Evaluate for Plasmodium parasites.
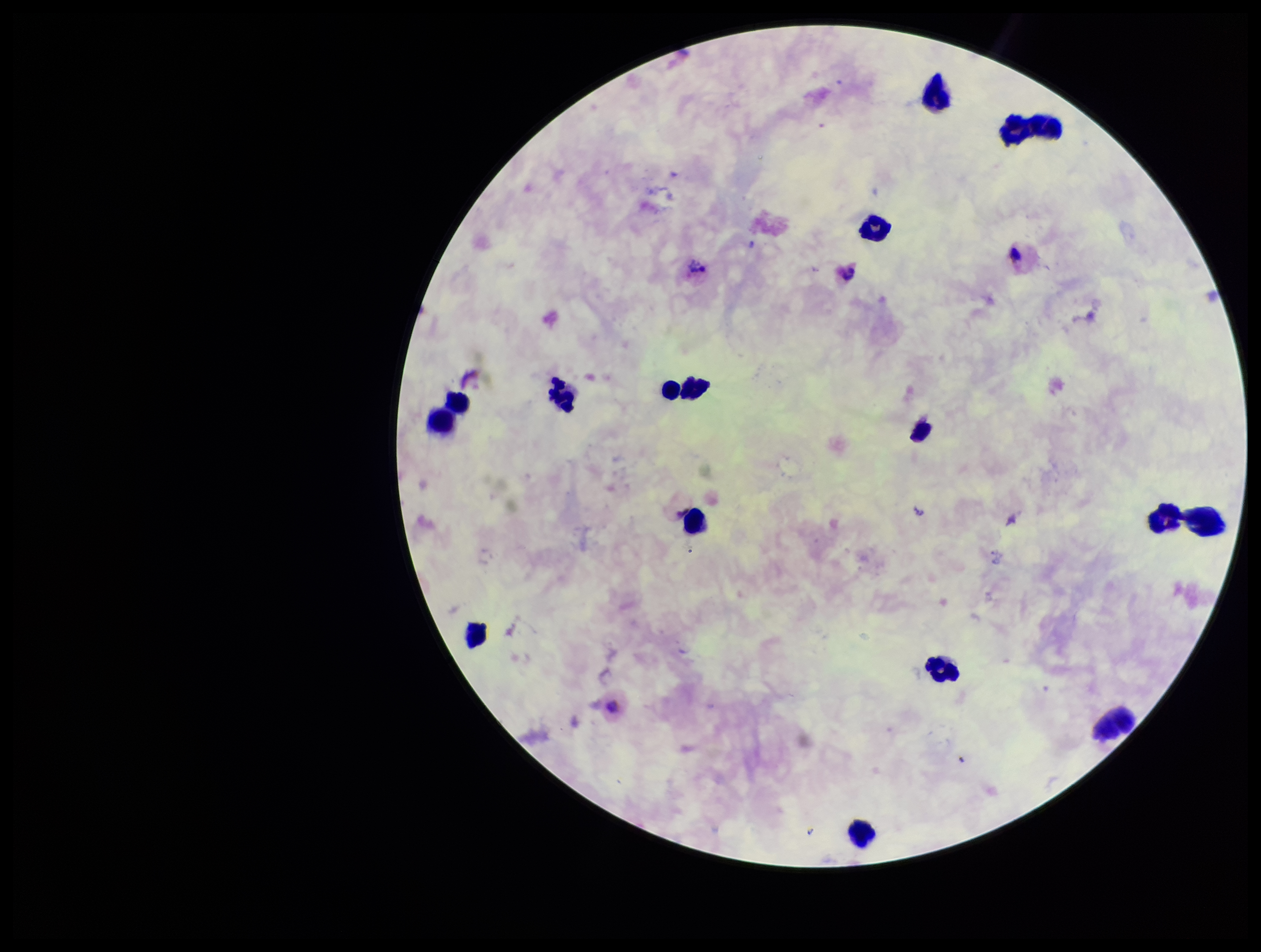

None seen.

Leukocyte count: 14. Stained with Giemsa. One field from this slide. Preparation: thick blood smear. Photographed through the microscope eyepiece with a smartphone camera. Image is 1261×952 pixels. Species reported for this patient: Plasmodium vivax. Parasite count: 0. Patient malaria status: infected.